State which cell type is depicted.
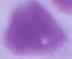

This is an erythrocyte.

{
  "modality": "photomicrograph",
  "magnification": "1000x"
}